Report the malaria status of this cell.
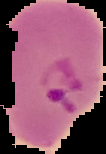

Parasitized.

image type = cell region segmented out of the field of view; surrounding area masked to black
preparation = thin blood smear
image size = 106×154 pixels